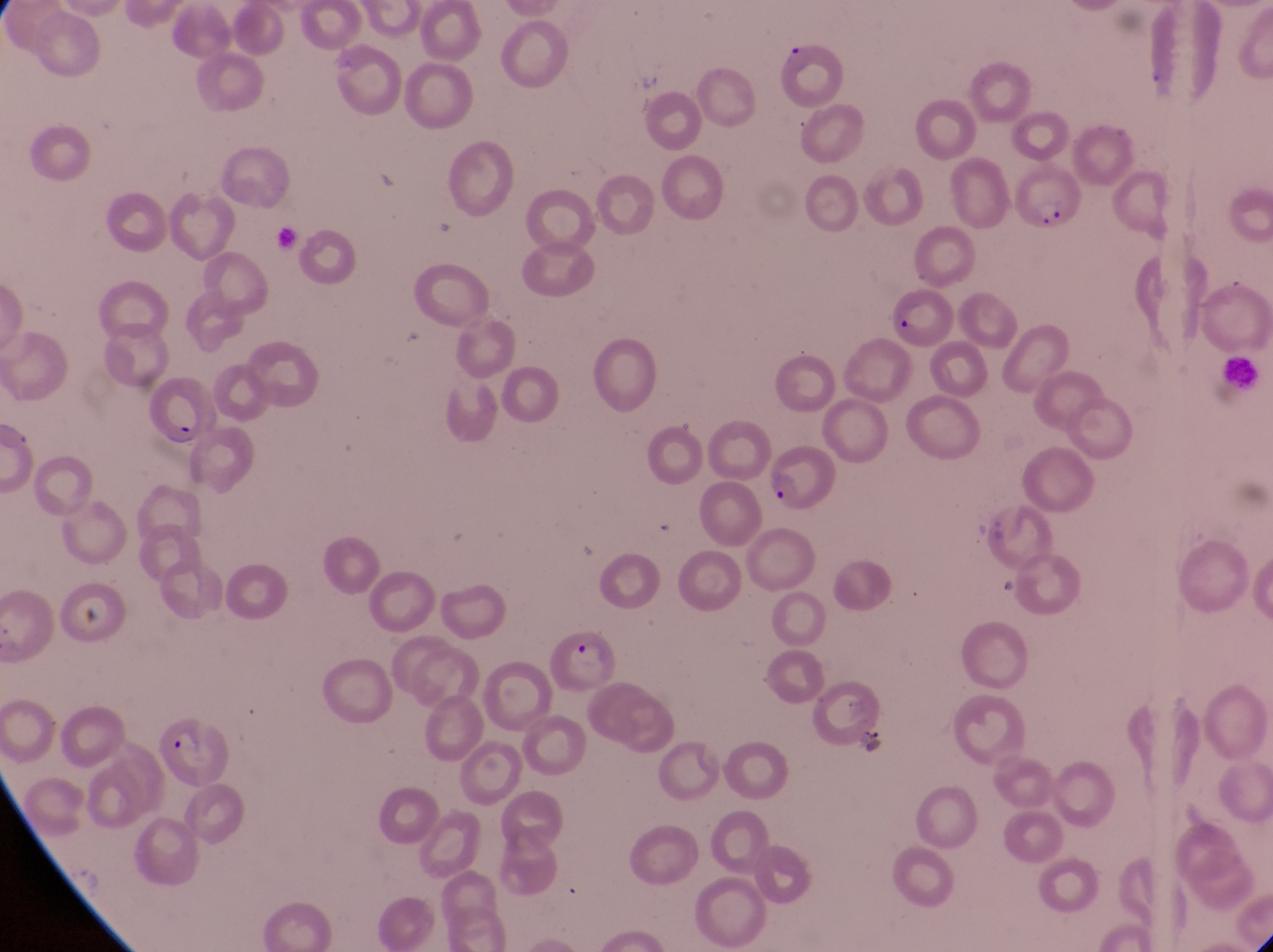 Approximate bounding boxes as (left, top, right, bottom) in pixels. Parasitised red blood cell locations: (1016, 165, 1090, 245), (142, 379, 217, 444), (768, 452, 842, 514), (546, 629, 618, 697), (160, 719, 232, 784). Leukocyte locations: (1221, 352, 1266, 393). Artifact (platelet-like body, stain precipitate, or debris) locations: (75, 609, 108, 644). Captured by a smartphone held over the eyepiece of an Olympus CX-23 microscope. Image is 1273×952 pixels. Collected in Uganda. Thin blood film. Magnification of 1000x. One field of view.